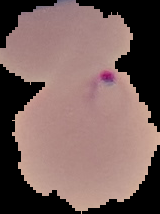
Summary:
  - Malaria status: parasitized
  - Preparation: thin blood smear
  - Image size: 160×214 pixels
  - Image type: cell region segmented out of the field of view; surrounding area masked to black